Classify this cell by malaria status.
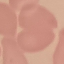
Uninfected.

Summary:
  - Preparation: thin smear
  - Capture: smartphone through the microscope eyepiece
  - Stain: Giemsa
  - Image type: automatically extracted cell patch, resized to 64 × 64 pixels